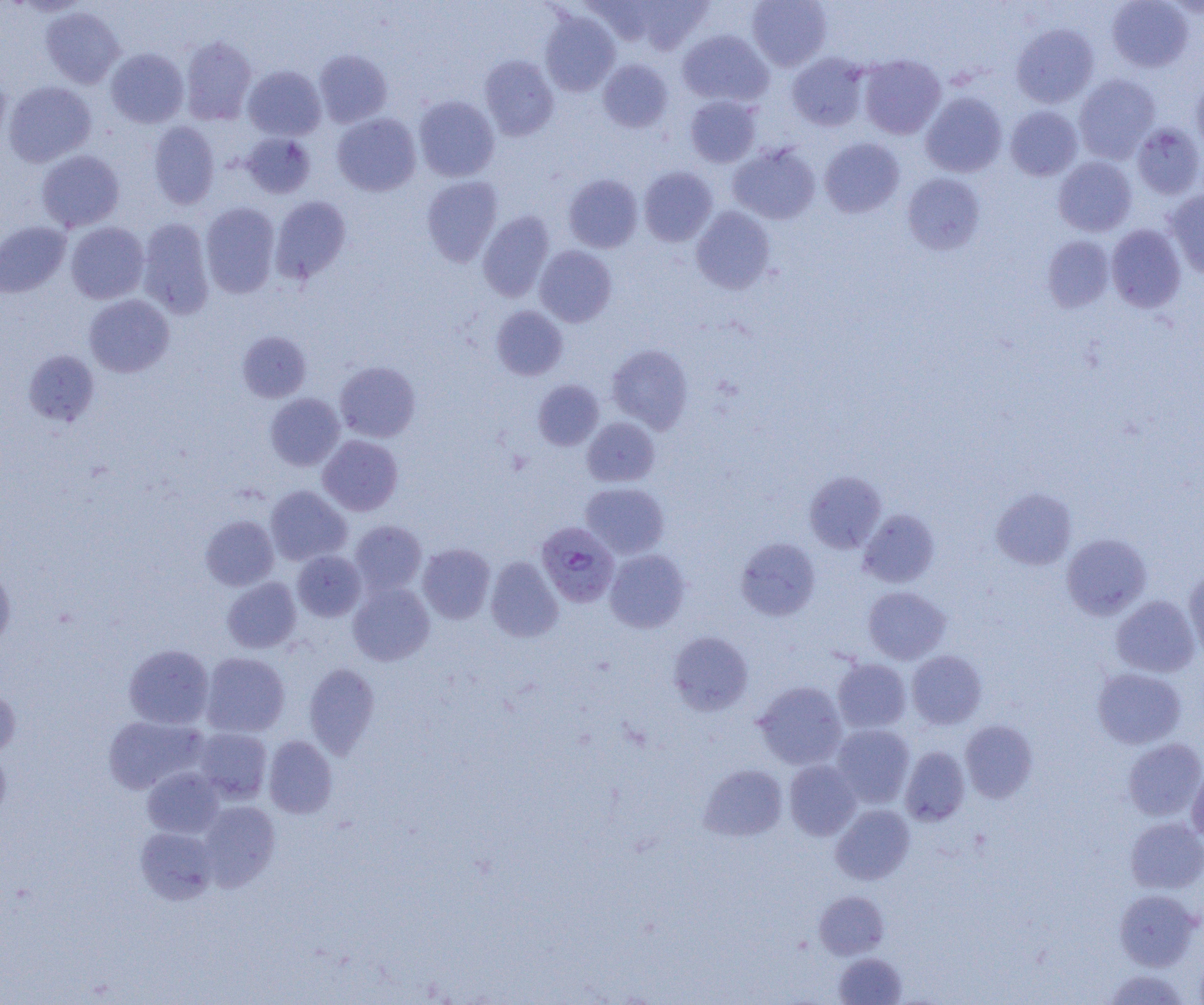

slide-level diagnosis = Plasmodium falciparum
image size = 1204×1005 pixels
uninfected red blood cell locations = approximate bounding boxes as [x1, y1, x2, y2] in pixels: [585, 0, 659, 45], [634, 0, 713, 54], [747, 0, 832, 71], [1107, 0, 1194, 72], [40, 6, 124, 88], [539, 11, 620, 96], [1012, 23, 1099, 107], [677, 29, 774, 107], [180, 36, 256, 124], [106, 48, 188, 128], [314, 49, 392, 127], [787, 53, 869, 131], [858, 54, 946, 139], [479, 55, 559, 141], [598, 59, 673, 133], [243, 66, 326, 140], [0, 69, 11, 148], [1073, 74, 1160, 163], [1191, 79, 1204, 155], [4, 81, 96, 167], [920, 92, 1007, 177], [685, 95, 761, 168], [414, 96, 499, 182], [1005, 106, 1082, 180], [332, 113, 421, 196], [149, 121, 219, 209], [1131, 123, 1204, 199], [241, 133, 315, 198], [819, 138, 904, 218], [728, 143, 820, 225], [36, 150, 124, 231], [1054, 156, 1137, 236], [638, 166, 717, 246], [902, 173, 985, 254], [564, 174, 642, 252], [422, 176, 503, 266], [1164, 190, 1204, 278], [271, 196, 351, 282], [201, 202, 280, 298], [691, 206, 775, 294], [478, 211, 554, 301], [137, 218, 214, 318], [0, 222, 70, 297], [66, 222, 149, 303], [1107, 224, 1186, 312], [1042, 236, 1114, 312], [535, 245, 617, 327], [84, 294, 174, 377], [491, 306, 567, 380], [238, 331, 311, 402], [606, 344, 693, 433], [24, 350, 99, 425], [335, 361, 420, 442], [533, 380, 604, 450], [265, 393, 344, 470], [582, 417, 660, 487], [318, 435, 403, 515], [804, 471, 887, 553], [580, 482, 669, 558], [266, 486, 352, 566], [991, 487, 1076, 570], [858, 509, 940, 588], [201, 516, 278, 591], [349, 520, 427, 595], [1062, 533, 1151, 619], [736, 537, 820, 620], [418, 543, 495, 623], [605, 549, 690, 632], [292, 550, 366, 621], [485, 556, 563, 642], [0, 567, 15, 649], [1184, 570, 1204, 659], [222, 578, 301, 653], [349, 583, 433, 666], [863, 586, 950, 664], [1111, 595, 1200, 678], [668, 631, 754, 716], [123, 645, 214, 729], [906, 650, 987, 729], [201, 652, 289, 737], [833, 659, 911, 732], [304, 663, 380, 758], [1093, 667, 1186, 749], [754, 681, 847, 770], [0, 686, 20, 759], [103, 715, 206, 794], [961, 720, 1037, 803], [831, 724, 915, 808], [194, 728, 272, 803], [263, 735, 337, 818], [1123, 738, 1204, 821], [0, 747, 11, 821], [900, 747, 970, 826], [784, 760, 861, 841], [699, 764, 788, 841], [142, 767, 224, 838], [1187, 767, 1204, 843], [198, 800, 281, 889], [831, 804, 915, 884], [1125, 818, 1204, 893], [136, 827, 218, 904], [1114, 889, 1201, 971], [814, 891, 889, 959], [834, 953, 907, 1004], [1193, 955, 1204, 1005], [1104, 969, 1189, 1004]
modality = light microscopy
magnification = 1000x
field of view = single
preparation = thin blood smear
Plasmodium falciparum-infected red blood cell locations = approximate bounding boxes as [x1, y1, x2, y2] in pixels: [536, 522, 620, 607]